Identify the preparation type.
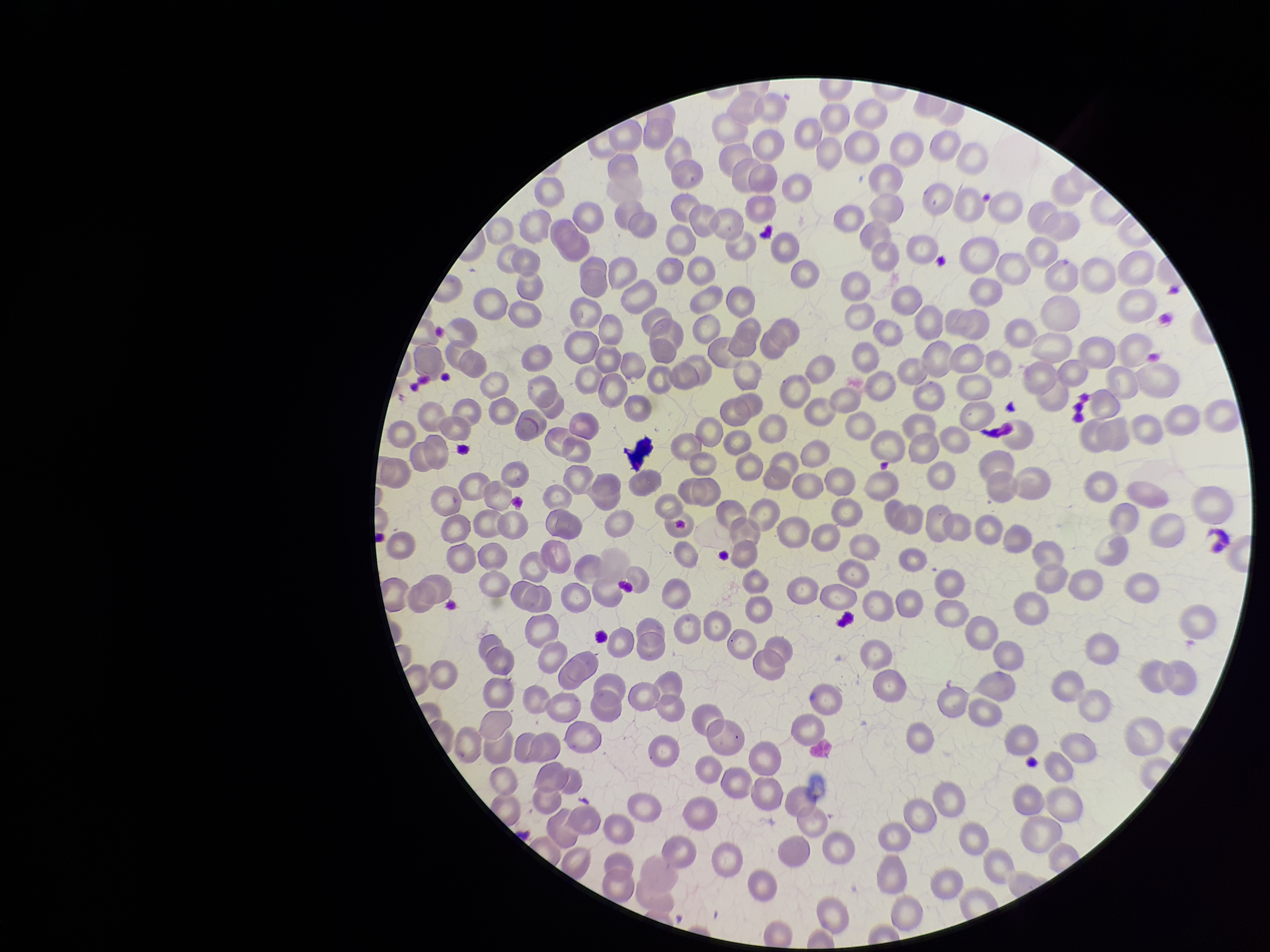

It is a thin blood smear.

Red blood cell count: 262. Parasitized red blood cell count: 0. Photographed through the microscope eyepiece with a smartphone camera. Parasitized red blood cells: none seen. Patient malaria status: negative. One field from this slide. Image is 1270×952 pixels. Giemsa stain.